Report the malaria status of this cell.
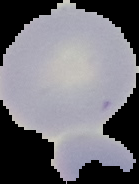
It is uninfected.

Cell region segmented out of the field of view; the surrounding area is masked to black. Image is 139×184 pixels. From a thin blood film.